Report the malaria status of this cell.
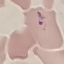
It is parasitized.

{
  "image_type": "automatically extracted cell patch, resized to 64 × 64 pixels",
  "capture": "smartphone through the microscope eyepiece",
  "stain": "Giemsa",
  "preparation": "thin smear"
}